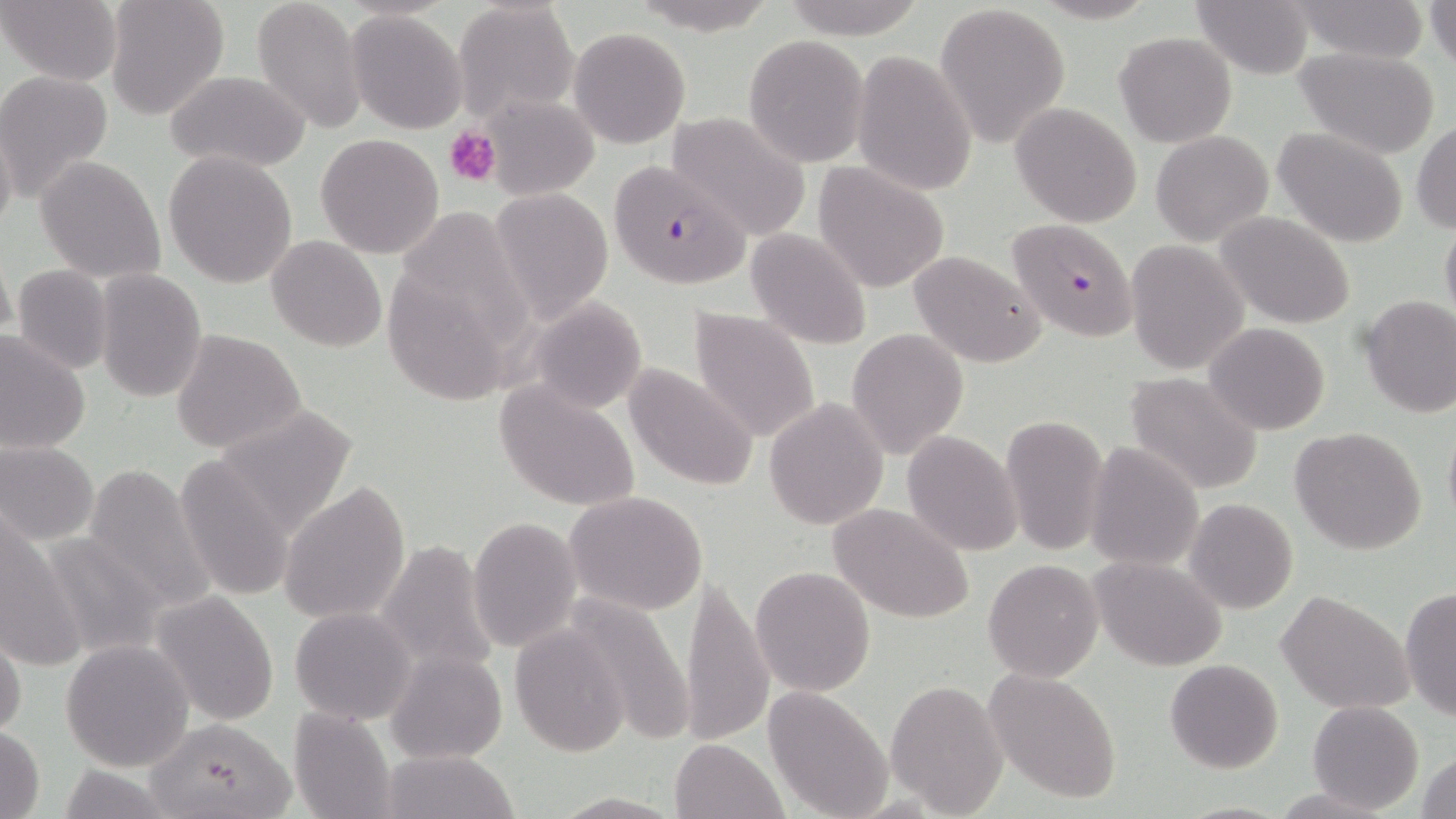
slide_level_diagnosis: Plasmodium falciparum
preparation: thin blood smear
plasmodium_falciparum_infected_red_blood_cell_locations: 'approximate bounding boxes as (x1,y1)-(x2,y2) corner pairs in pixels: (607,164)-(748,291), (1007,216)-(1137,342)'
stain: May-Grünwald-Giemsa
modality: optical microscopy
field_of_view: one of a larger specimen
platelet_locations: 'approximate bounding boxes as (x1,y1)-(x2,y2) corner pairs in pixels: (444,126)-(500,187)'
uninfected_red_blood_cell_locations: 'approximate bounding boxes as (x1,y1)-(x2,y2) corner pairs in pixels: (2,0)-(122,86), (104,0)-(228,118), (251,0)-(367,133), (781,0)-(926,38), (1192,0)-(1317,77), (1292,0)-(1431,62), (1426,0)-(1455,73), (454,1)-(580,121), (935,2)-(1071,147), (346,8)-(467,132), (568,27)-(689,148), (1113,30)-(1237,147), (743,35)-(870,166), (1297,49)-(1439,159), (850,51)-(978,195), (0,70)-(114,200), (165,72)-(310,172), (483,92)-(599,200), (1011,102)-(1142,227), (665,111)-(811,240), (0,119)-(17,242), (1412,121)-(1456,234), (1273,127)-(1409,247), (1151,129)-(1274,246), (316,132)-(445,259), (162,150)-(297,288), (35,157)-(165,282), (812,161)-(950,294), (490,188)-(615,323), (1217,212)-(1357,329), (1440,219)-(1456,329), (745,227)-(872,349), (267,235)-(386,352), (1127,240)-(1248,375), (1,244)-(16,349), (906,249)-(1047,367), (12,264)-(114,375), (96,269)-(208,402), (1358,294)-(1455,418), (525,295)-(649,412), (688,307)-(822,445), (1205,323)-(1331,436), (846,327)-(970,460), (171,329)-(306,455), (0,330)-(90,452), (623,362)-(759,493), (1124,372)-(1264,495), (494,378)-(640,514), (764,397)-(889,529), (209,403)-(359,540), (999,416)-(1108,555), (1442,419)-(1456,536), (1289,426)-(1428,554), (902,430)-(1022,556), (0,439)-(100,546), (1086,442)-(1203,573), (174,456)-(295,603), (83,462)-(215,614), (280,481)-(412,626), (563,490)-(708,616), (1186,498)-(1298,614), (828,502)-(975,624), (2,516)-(78,666), (467,516)-(582,654), (40,531)-(167,659), (373,536)-(501,681), (1091,556)-(1227,671), (982,558)-(1104,682), (750,566)-(876,697), (680,571)-(775,747), (1399,586)-(1456,721), (149,590)-(281,725), (1276,590)-(1414,714), (559,591)-(695,746), (289,607)-(417,725), (510,623)-(630,755), (0,627)-(25,742), (60,638)-(194,773), (385,651)-(507,764), (1164,658)-(1283,772), (982,668)-(1124,805), (886,678)-(1008,814), (761,687)-(892,819), (1308,700)-(1424,814), (288,707)-(396,819), (143,716)-(298,818), (0,725)-(47,818), (670,738)-(787,819), (381,748)-(518,819), (1415,749)-(1456,819), (55,764)-(178,818), (551,792)-(683,819)'
magnification: 1000x
image_size: 1456×819 pixels